Report the malaria status of this cell.
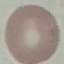
Uninfected.

Summary:
  - Preparation: thin smear
  - Stain: Giemsa
  - Capture: smartphone camera at the microscope eyepiece
  - Image type: automatically extracted cell patch, resized to 64 × 64 pixels